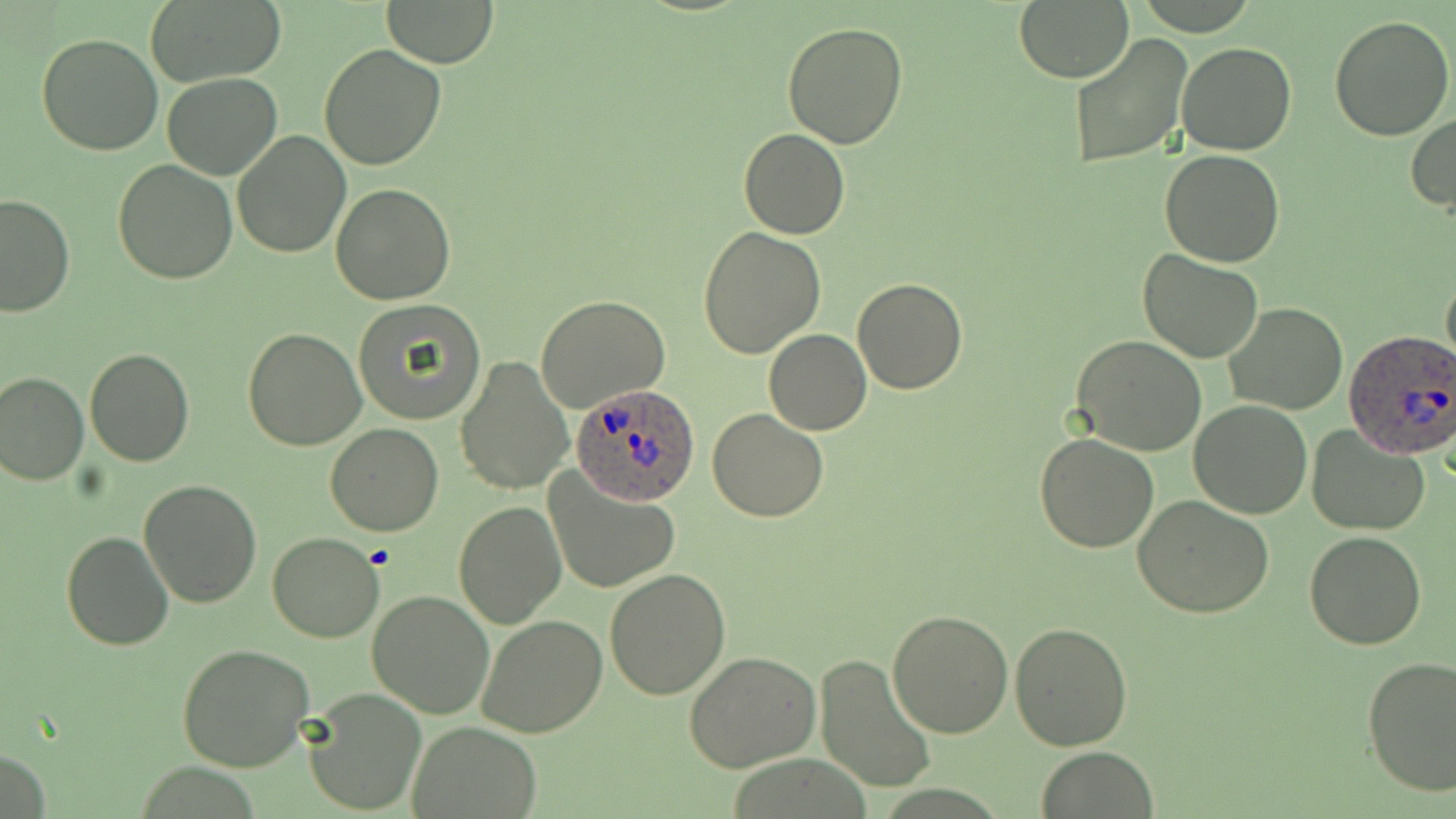
Approximate bounding boxes as (x1, y1, x2, y2) in pixels. Plasmodium ovale-infected red blood cell locations: (1345, 331, 1456, 460), (570, 383, 703, 508). Uninfected red blood cell locations: (140, 0, 287, 88), (1013, 0, 1134, 84), (381, 1, 501, 66), (1329, 13, 1455, 140), (783, 22, 910, 149), (36, 31, 164, 156), (1068, 33, 1193, 169), (1175, 41, 1296, 157), (320, 43, 447, 170), (162, 73, 283, 180), (1407, 113, 1456, 215), (739, 128, 849, 239), (231, 129, 351, 259), (1161, 149, 1285, 266), (112, 159, 238, 284), (331, 181, 456, 304), (0, 193, 77, 316), (696, 227, 825, 360), (1137, 250, 1264, 364), (1441, 268, 1456, 374), (853, 278, 967, 393), (536, 295, 672, 413), (353, 301, 486, 425), (1223, 303, 1350, 416), (243, 326, 366, 449), (764, 329, 872, 435), (1072, 336, 1208, 457), (84, 346, 194, 466), (455, 355, 573, 496), (0, 370, 89, 485), (1190, 399, 1312, 519), (708, 409, 828, 522), (324, 423, 444, 536), (1306, 425, 1430, 536), (1034, 432, 1160, 552), (543, 471, 680, 595), (139, 480, 264, 608), (1133, 494, 1275, 618), (454, 500, 565, 629), (61, 530, 174, 651), (1303, 531, 1427, 650), (266, 532, 383, 642), (604, 569, 730, 701), (366, 591, 495, 719), (886, 608, 1015, 738), (475, 615, 607, 739), (1009, 623, 1134, 750), (177, 644, 313, 772), (684, 651, 824, 771), (813, 653, 938, 795), (1360, 655, 1456, 796), (303, 687, 428, 816), (409, 722, 540, 815), (1035, 747, 1159, 818). Slide-level diagnosis: Plasmodium ovale. 1000x magnification. Image is 1456×819 pixels. Thin blood smear. May-Grünwald-Giemsa stain. One field of a larger specimen. Optical microscopy.